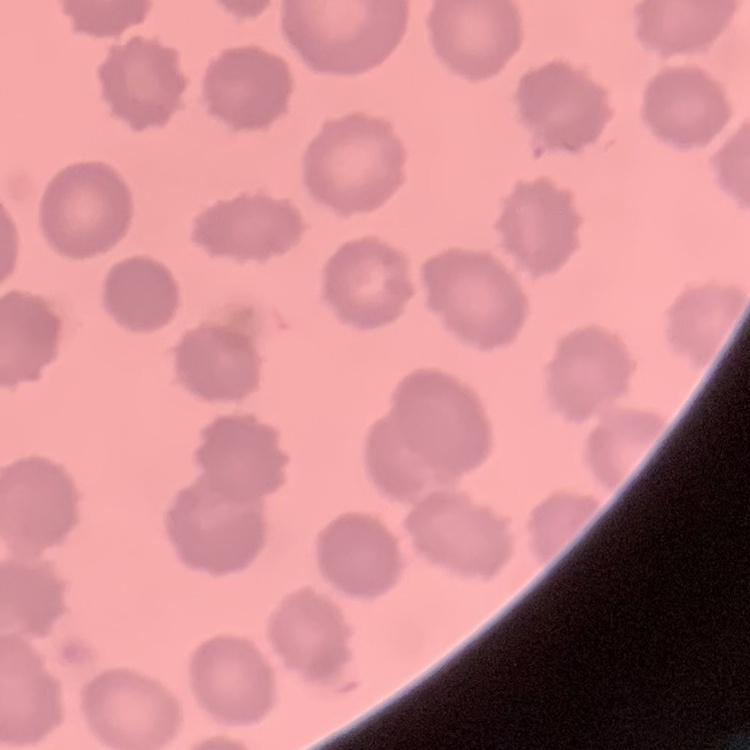
The erythrocytes exhibit no rouleaux formation. One tile cut from a larger photomicrograph. Stained with either Field's or Giemsa. Thin blood smear.